Report the malaria status of this cell.
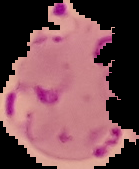

Parasitized.

{
  "image_size": "139×169 pixels",
  "preparation": "thin blood film",
  "image_type": "segmented cell region with the area outside set to black"
}